Assess this cell for malaria.
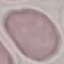

It is uninfected.

Summary:
  - Preparation: thin smear
  - Image type: cell patch, automatically extracted from a larger field of view and resized to 64 × 64 pixels
  - Stain: Giemsa
  - Capture: smartphone through the microscope eyepiece